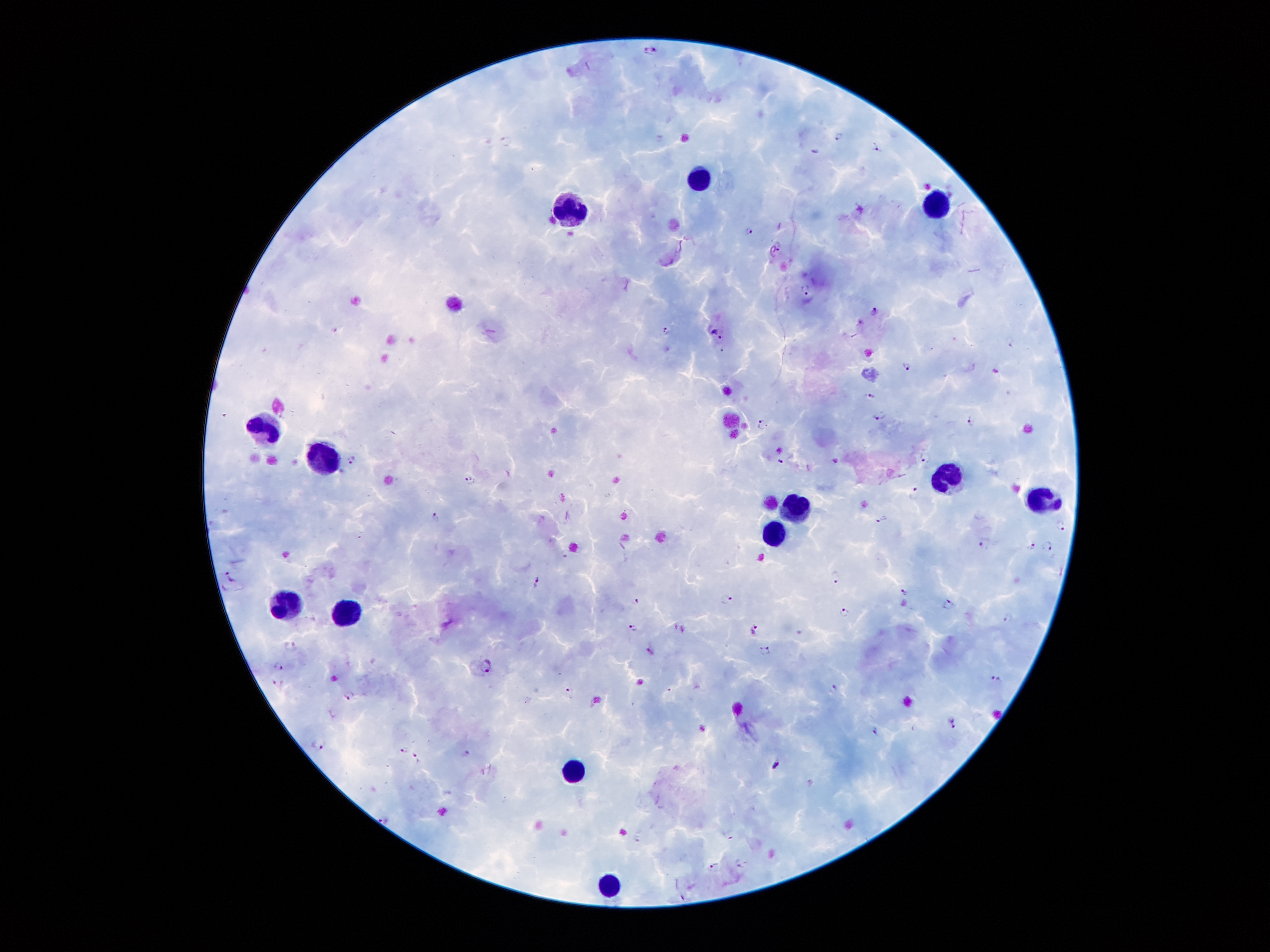

coordinate format = approximate centers as (x, y) in pixels
Plasmodium parasite locations = (651, 50), (838, 135), (877, 148), (751, 230), (779, 244), (806, 288), (875, 309), (668, 330), (716, 333), (1010, 341), (906, 365), (870, 396), (880, 414), (970, 419), (762, 425), (926, 458), (353, 460), (781, 462), (471, 480), (913, 493), (435, 517), (882, 519), (1059, 526), (985, 542), (1030, 546), (1047, 548), (231, 574), (835, 578), (536, 581), (904, 593), (726, 598), (636, 600), (948, 604), (844, 613), (1009, 619), (633, 628), (755, 629), (290, 645), (650, 649), (766, 650), (279, 666), (486, 666), (995, 680), (277, 684), (833, 688), (570, 692), (348, 694), (953, 723), (874, 730), (319, 743), (403, 751), (418, 760), (777, 765), (384, 818), (731, 834), (739, 862), (714, 865)
leukocyte locations = (696, 181), (935, 202), (578, 209), (260, 431), (326, 458), (953, 475), (1038, 495), (804, 506), (772, 534), (290, 603), (347, 612), (571, 771), (610, 885)
stain = Giemsa
patient malaria status = infected with Plasmodium falciparum
field of view = one from this slide
capture = smartphone camera through the microscope eyepiece
image size = 1270×952 pixels
preparation = thick peripheral-blood smear
magnification = 100x